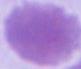

identification = erythrocyte
modality = photomicrograph
magnification = 1000x